Locate every Plasmodium parasite.
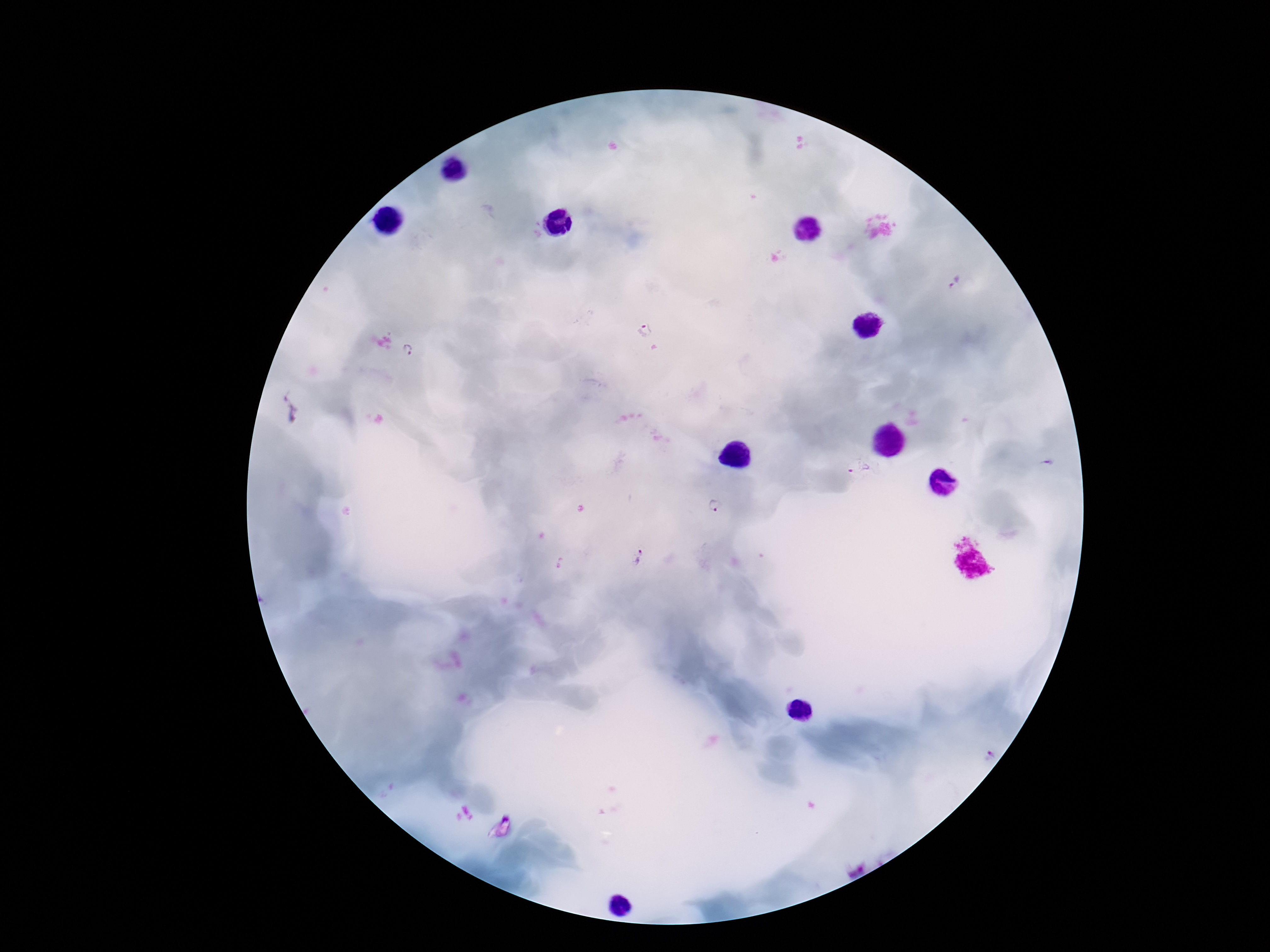

Approximate centers as (x, y) in pixels.
Plasmodium parasites: (955, 282), (644, 330), (409, 351), (860, 468), (714, 505), (638, 557).

capture = smartphone camera through the microscope eyepiece
field of view = one from this slide
preparation = thick peripheral-blood smear
magnification = 100x
stain = Giemsa
image size = 1270×952 pixels
patient malaria status = infected